Describe the morphology of the erythrocytes.
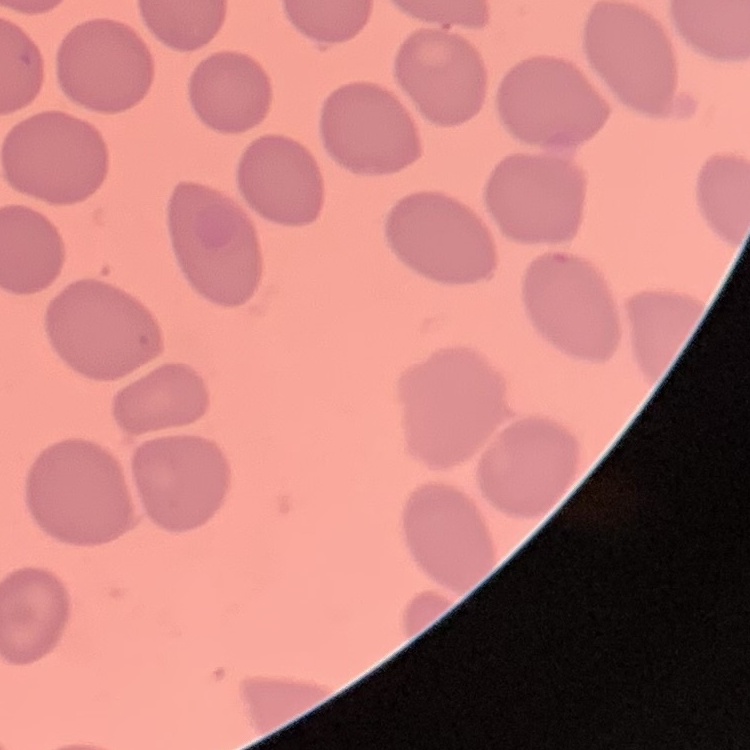
No rouleaux formation.

stain = Field's or Giemsa
preparation = thin blood smear
image type = one tile cut from a larger photomicrograph